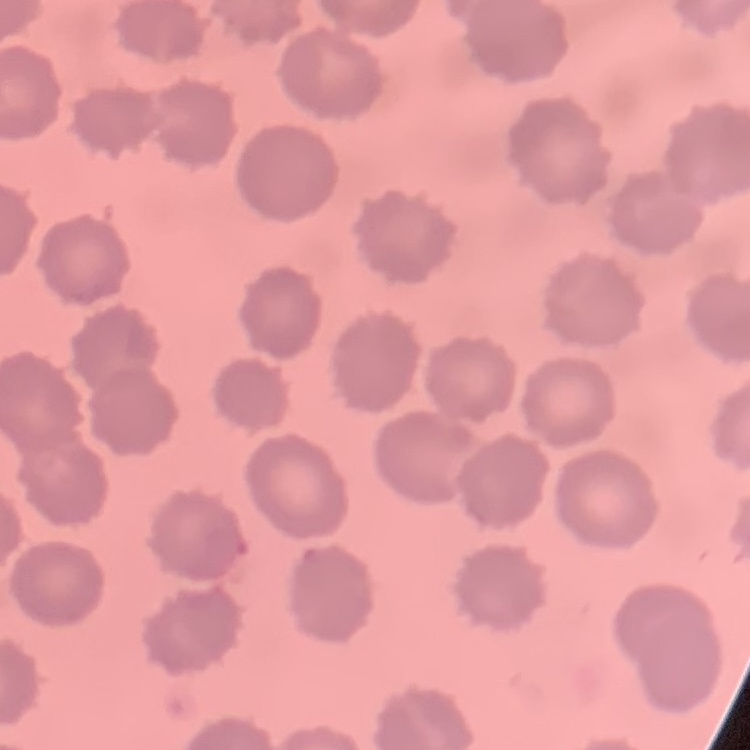
Summary:
  - Erythrocyte morphology: no rouleaux formation
  - Preparation: thin blood film
  - Stain: Field's or Giemsa
  - Image type: square crop of a larger photomicrograph